Report the malaria status of this cell.
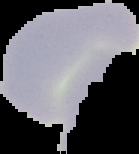

Uninfected.

Segmented cell region on a black background. Image is 139×154 pixels. From a thin blood smear.